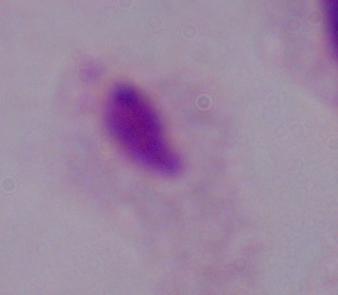

magnification: 1000x
modality: photomicrograph
identification: trichomonad